Classify this cell by malaria status.
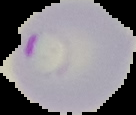
It is parasitized.

From a thin blood smear. Segmented cell region on a black background. Image is 136×115 pixels.